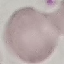

Summary:
  - Result: no malaria parasites detected
  - Image type: automatically extracted cell patch, resized to 64 × 64 pixels
  - Capture: smartphone camera at the microscope eyepiece
  - Preparation: thin blood film
  - Stain: Giemsa